Report the malaria status of this cell.
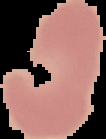

Uninfected.

image size = 106×139 pixels
image type = cell region segmented out of the field of view; surrounding area masked to black
preparation = thin blood smear